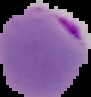

The area outside the segmented cell region is set to black. Malaria status: parasitized. From a thin blood smear. Image is 91×97 pixels.